Describe the morphology of the red blood cells.
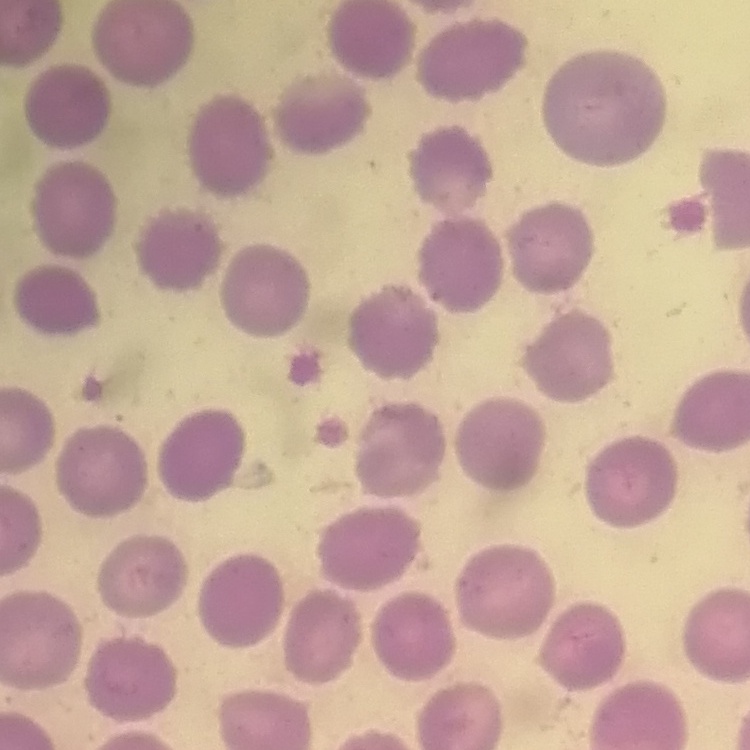
They show no rouleaux formation.

Square crop of a larger photomicrograph. Thin peripheral smear. Stained with either Field's or Giemsa.